Assess for Plasmodium parasites.
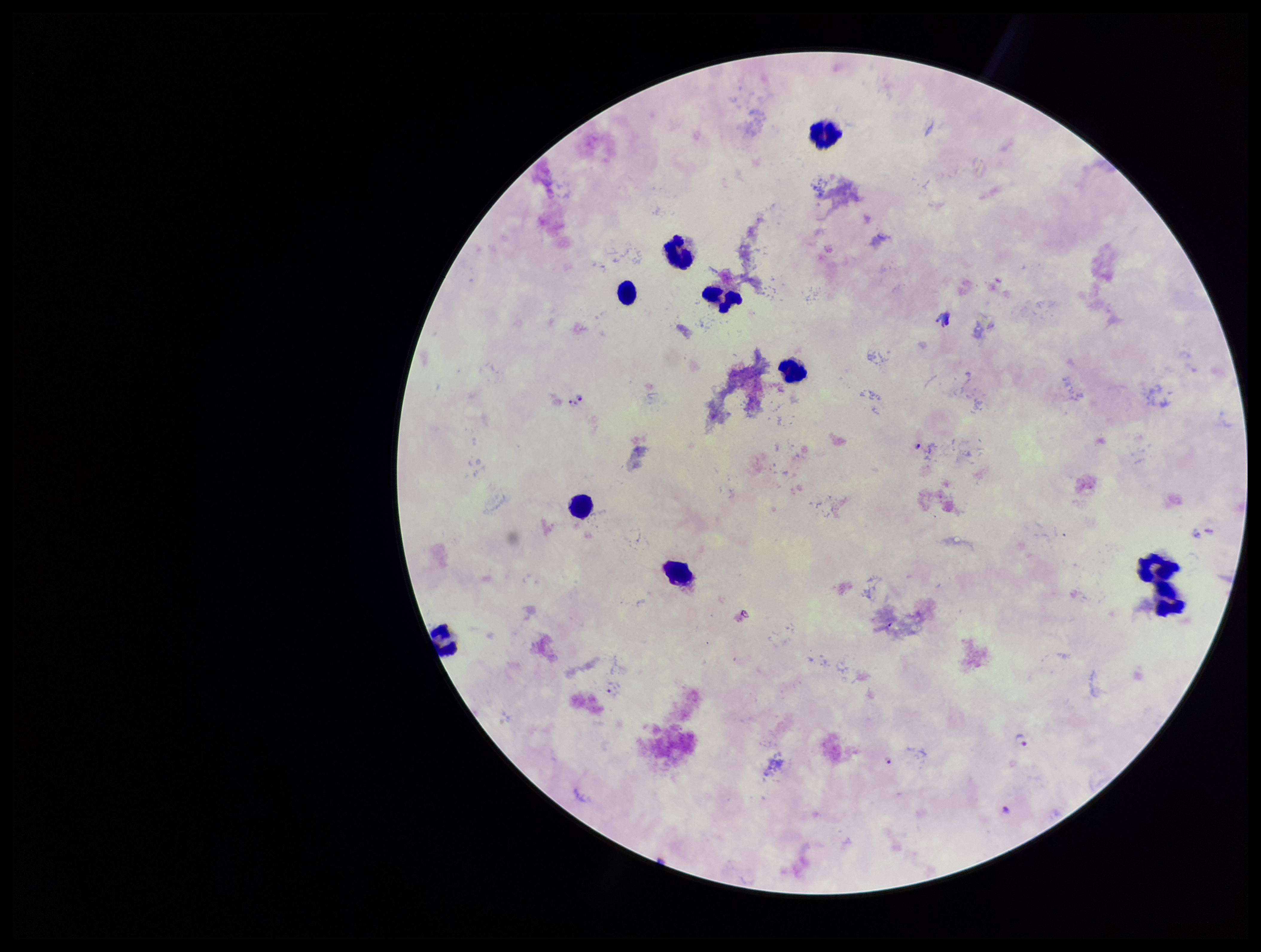

Identified.

Summary:
  - Field of view: one from this slide
  - Image size: 1261×952 pixels
  - Parasite count: 8
  - Capture: smartphone photograph through the microscope eyepiece
  - Leukocyte count: 10
  - Preparation: thick
  - Stain: Giemsa
  - Patient malaria status: infected
  - Species reported for this patient: Plasmodium falciparum